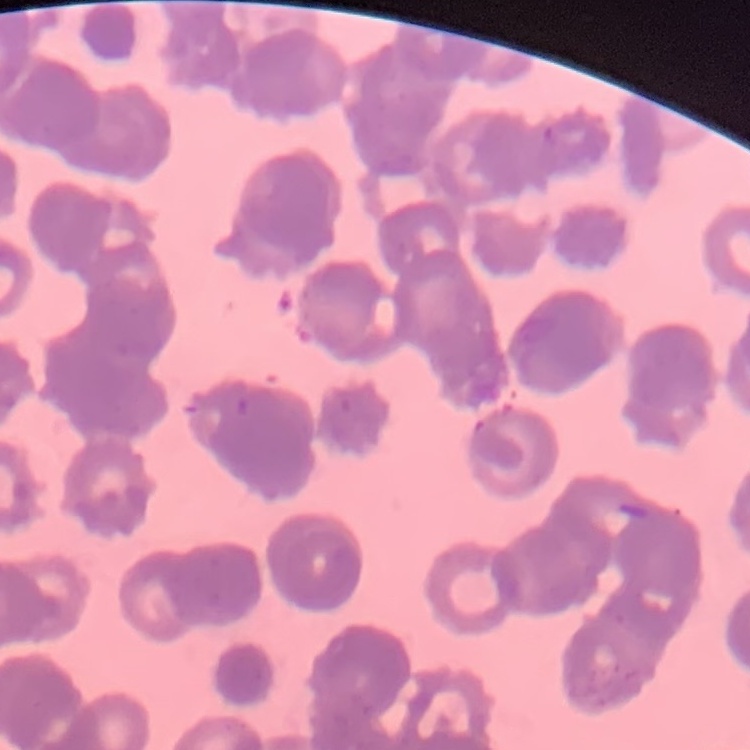
red blood cell morphology = rouleaux formation
preparation = thin peripheral smear
image type = one tile cut from a larger photomicrograph
stain = Field's or Giemsa